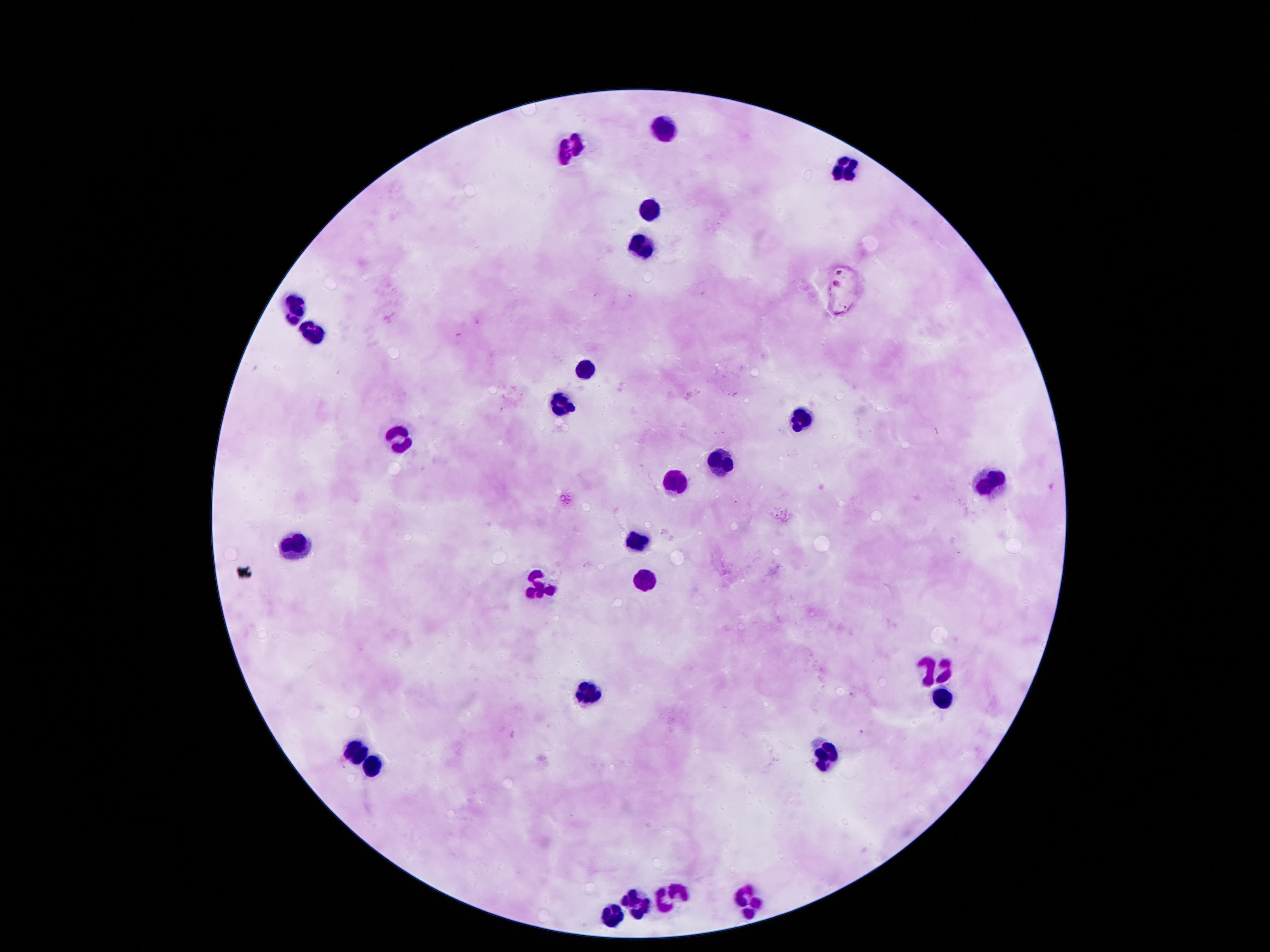
preparation = thick blood smear
magnification = 100x
stain = Giemsa
patient malaria status = not infected
image size = 1270×952 pixels
leukocyte locations = approximate centers as [x, y] in pixels: [661, 128], [566, 154], [842, 164], [649, 205], [641, 242], [298, 309], [313, 333], [590, 363], [557, 404], [800, 418], [398, 439], [720, 461], [989, 477], [670, 485], [637, 541], [295, 545], [641, 582], [539, 585], [944, 667], [593, 690], [942, 700], [826, 751], [358, 754], [376, 767], [670, 893], [747, 903], [636, 904], [613, 915]
capture = smartphone camera through the microscope eyepiece
field of view = single